Report the malaria status of this cell.
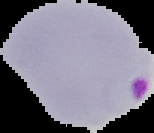

It is parasitized.

From a thin blood smear. Segmented cell region on a black background. Image is 154×133 pixels.